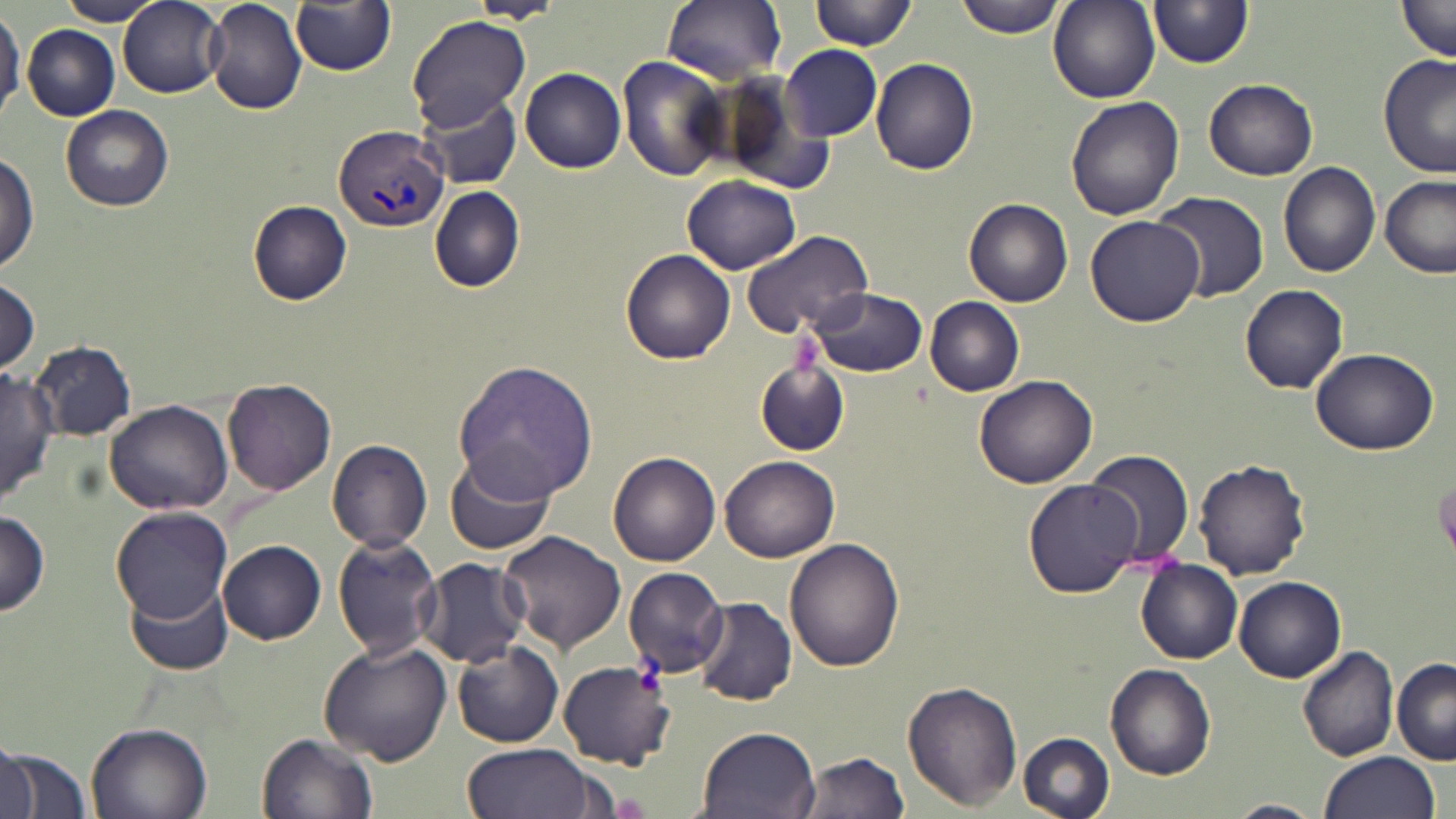
slide-level diagnosis = Plasmodium vivax
stain = May-Grünwald-Giemsa
modality = optical microscopy
field of view = single
uninfected red blood cell locations = approximate bounding boxes as [x1, y1, x2, y2] in pixels: [54, 0, 166, 25], [291, 0, 396, 75], [662, 0, 788, 84], [811, 0, 916, 51], [953, 0, 1068, 38], [1047, 0, 1159, 104], [1395, 0, 1455, 64], [119, 1, 226, 99], [204, 1, 308, 115], [1149, 1, 1253, 70], [467, 2, 564, 25], [0, 8, 23, 120], [19, 14, 224, 112], [407, 14, 530, 129], [22, 24, 119, 119], [780, 44, 883, 141], [1377, 55, 1454, 178], [617, 56, 730, 182], [870, 59, 978, 176], [520, 67, 626, 174], [1204, 77, 1319, 180], [415, 90, 522, 190], [1065, 96, 1185, 221], [61, 106, 174, 212], [0, 154, 38, 272], [1278, 162, 1382, 278], [682, 175, 802, 275], [1379, 175, 1456, 278], [429, 185, 525, 291], [1150, 190, 1269, 306], [964, 197, 1074, 309], [248, 200, 353, 305], [1085, 214, 1206, 326], [740, 229, 876, 344], [621, 248, 736, 364], [0, 280, 41, 376], [1240, 284, 1349, 393], [806, 288, 928, 377], [925, 297, 1026, 396], [31, 340, 135, 439], [1309, 347, 1438, 455], [453, 359, 597, 502], [754, 361, 849, 457], [0, 368, 59, 502], [975, 374, 1098, 489], [223, 376, 336, 495], [106, 400, 232, 514], [327, 439, 431, 551], [1085, 448, 1195, 573], [441, 449, 556, 558], [607, 451, 720, 566], [719, 454, 838, 564], [1192, 458, 1311, 579], [1023, 480, 1141, 598], [111, 505, 232, 621], [0, 510, 50, 616], [498, 530, 626, 653], [332, 533, 443, 660], [785, 537, 905, 671], [219, 540, 327, 644], [416, 557, 531, 669], [1136, 559, 1242, 664], [623, 566, 729, 679], [1234, 577, 1347, 681], [128, 578, 234, 676], [692, 596, 795, 706], [319, 640, 452, 765], [450, 641, 563, 747], [1297, 644, 1399, 762], [1391, 656, 1456, 765], [558, 659, 675, 769], [1105, 664, 1216, 780], [901, 680, 1020, 810], [85, 722, 212, 818], [694, 724, 821, 818], [257, 731, 378, 819], [1017, 732, 1114, 818], [0, 739, 38, 819], [461, 743, 595, 819], [2, 747, 93, 817], [1314, 749, 1440, 817], [793, 750, 912, 818], [1219, 799, 1322, 818]
preparation = thin blood smear
Plasmodium vivax-infected red blood cell locations = approximate bounding boxes as [x1, y1, x2, y2] in pixels: [335, 124, 449, 235]
image size = 1456×819 pixels
magnification = 1000x